Locate every blood parasite and identify its species.
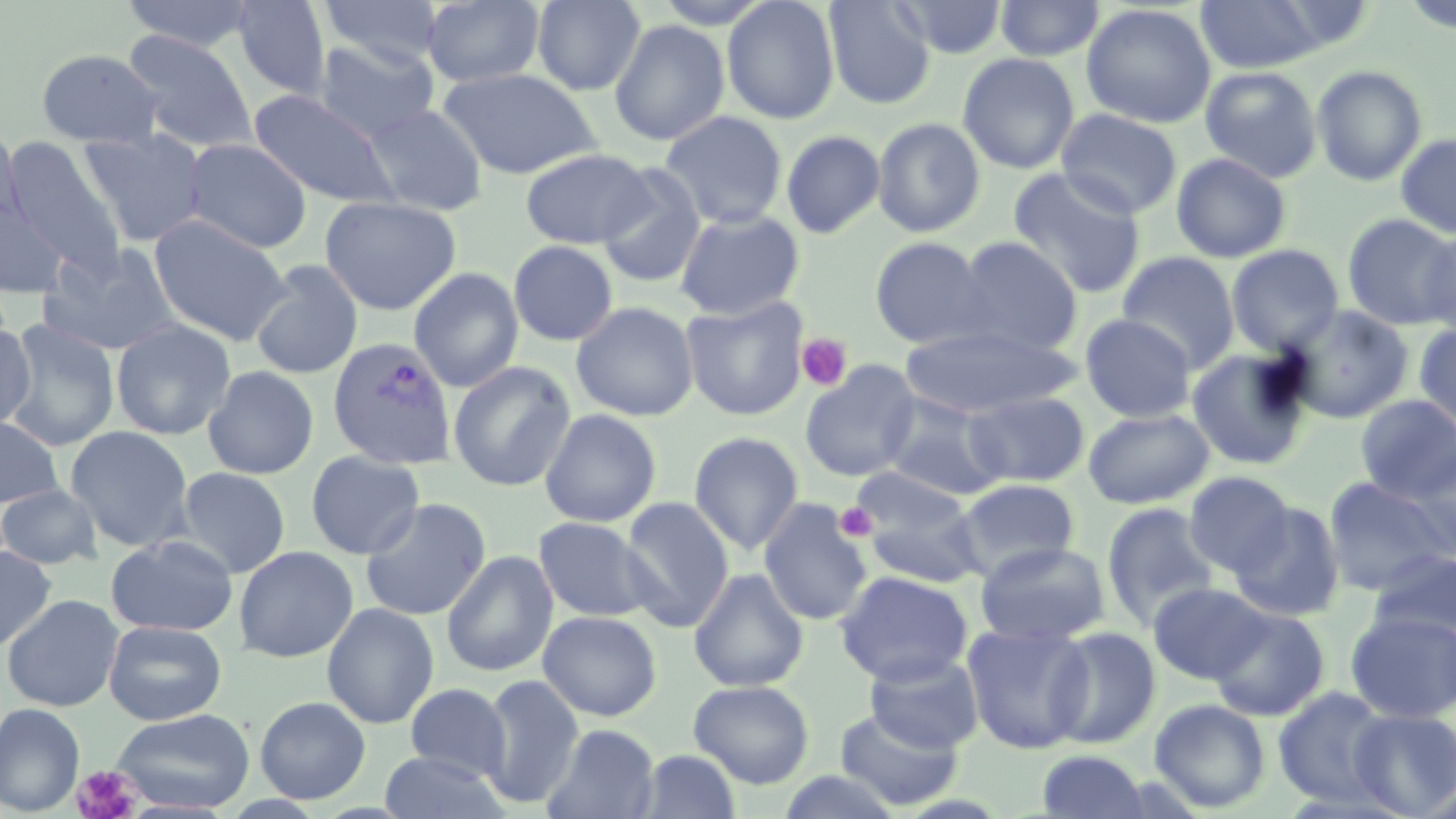
Approximate bounding boxes as named x1/y1/x2/y2 corners in pixels.
Plasmodium vivax-infected red blood cells: (x1=327, y1=334, x2=457, y2=469).
No Plasmodium falciparum, Plasmodium ovale, Plasmodium malariae, Babesia divergens, or Trypanosoma brucei observed.

Uninfected red blood cell locations: (x1=121, y1=0, x2=259, y2=52), (x1=231, y1=0, x2=332, y2=99), (x1=318, y1=0, x2=445, y2=68), (x1=531, y1=0, x2=646, y2=95), (x1=721, y1=0, x2=840, y2=124), (x1=823, y1=0, x2=935, y2=109), (x1=892, y1=0, x2=1008, y2=59), (x1=994, y1=0, x2=1105, y2=62), (x1=1195, y1=0, x2=1325, y2=73), (x1=421, y1=1, x2=545, y2=88), (x1=650, y1=1, x2=777, y2=28), (x1=1081, y1=3, x2=1217, y2=128), (x1=609, y1=19, x2=730, y2=146), (x1=121, y1=30, x2=258, y2=155), (x1=314, y1=37, x2=440, y2=142), (x1=36, y1=48, x2=163, y2=148), (x1=957, y1=52, x2=1080, y2=174), (x1=1311, y1=64, x2=1427, y2=187), (x1=1199, y1=66, x2=1323, y2=183), (x1=437, y1=67, x2=601, y2=179), (x1=248, y1=89, x2=397, y2=208), (x1=362, y1=103, x2=487, y2=216), (x1=1055, y1=108, x2=1182, y2=218), (x1=659, y1=111, x2=788, y2=229), (x1=872, y1=117, x2=987, y2=238), (x1=78, y1=126, x2=209, y2=247), (x1=0, y1=128, x2=24, y2=234), (x1=781, y1=129, x2=885, y2=239), (x1=1395, y1=132, x2=1456, y2=239), (x1=3, y1=137, x2=127, y2=277), (x1=182, y1=137, x2=313, y2=254), (x1=520, y1=147, x2=653, y2=249), (x1=1171, y1=152, x2=1291, y2=263), (x1=594, y1=165, x2=707, y2=290), (x1=1008, y1=167, x2=1147, y2=298), (x1=319, y1=195, x2=461, y2=316), (x1=1, y1=197, x2=69, y2=298), (x1=675, y1=208, x2=805, y2=320), (x1=149, y1=213, x2=291, y2=346), (x1=1341, y1=213, x2=1455, y2=330), (x1=1420, y1=227, x2=1456, y2=338), (x1=868, y1=236, x2=993, y2=349), (x1=955, y1=236, x2=1083, y2=355), (x1=508, y1=240, x2=618, y2=347), (x1=39, y1=243, x2=183, y2=356), (x1=1226, y1=244, x2=1344, y2=358), (x1=1117, y1=252, x2=1240, y2=370), (x1=249, y1=260, x2=364, y2=380), (x1=408, y1=267, x2=524, y2=393), (x1=681, y1=296, x2=809, y2=421), (x1=571, y1=301, x2=699, y2=421), (x1=1284, y1=304, x2=1414, y2=423), (x1=1080, y1=313, x2=1197, y2=421), (x1=2, y1=319, x2=120, y2=452), (x1=111, y1=319, x2=236, y2=440), (x1=0, y1=320, x2=36, y2=432), (x1=1413, y1=323, x2=1456, y2=427), (x1=899, y1=324, x2=1077, y2=419), (x1=1187, y1=347, x2=1313, y2=470), (x1=447, y1=360, x2=577, y2=492), (x1=799, y1=361, x2=923, y2=482), (x1=202, y1=365, x2=320, y2=480), (x1=964, y1=390, x2=1089, y2=487), (x1=1354, y1=394, x2=1456, y2=503), (x1=881, y1=396, x2=1006, y2=499), (x1=539, y1=408, x2=662, y2=527), (x1=1083, y1=408, x2=1214, y2=509), (x1=0, y1=415, x2=64, y2=510), (x1=64, y1=425, x2=194, y2=552), (x1=688, y1=431, x2=805, y2=555), (x1=1407, y1=449, x2=1455, y2=559), (x1=305, y1=450, x2=426, y2=560), (x1=175, y1=467, x2=291, y2=578), (x1=851, y1=467, x2=974, y2=548), (x1=1184, y1=471, x2=1295, y2=577), (x1=1323, y1=476, x2=1453, y2=595), (x1=953, y1=478, x2=1080, y2=579), (x1=0, y1=484, x2=103, y2=570), (x1=860, y1=488, x2=986, y2=588), (x1=620, y1=495, x2=735, y2=633), (x1=359, y1=496, x2=492, y2=621), (x1=758, y1=498, x2=873, y2=627), (x1=1102, y1=502, x2=1220, y2=631), (x1=1230, y1=502, x2=1346, y2=621), (x1=533, y1=516, x2=656, y2=622), (x1=105, y1=534, x2=238, y2=636), (x1=974, y1=541, x2=1110, y2=646), (x1=0, y1=545, x2=57, y2=652), (x1=233, y1=545, x2=359, y2=663), (x1=1365, y1=548, x2=1456, y2=646), (x1=440, y1=550, x2=558, y2=677), (x1=688, y1=568, x2=809, y2=692), (x1=834, y1=570, x2=973, y2=686), (x1=1149, y1=582, x2=1270, y2=685), (x1=1, y1=594, x2=124, y2=712), (x1=321, y1=602, x2=440, y2=729), (x1=1209, y1=607, x2=1330, y2=721), (x1=538, y1=610, x2=662, y2=721), (x1=1345, y1=612, x2=1456, y2=723), (x1=103, y1=619, x2=227, y2=725), (x1=963, y1=621, x2=1093, y2=754), (x1=1045, y1=625, x2=1161, y2=749), (x1=863, y1=652, x2=984, y2=754), (x1=479, y1=673, x2=584, y2=808), (x1=688, y1=679, x2=814, y2=788), (x1=404, y1=683, x2=512, y2=781), (x1=1272, y1=686, x2=1396, y2=808), (x1=254, y1=696, x2=372, y2=804), (x1=1149, y1=698, x2=1270, y2=812), (x1=0, y1=703, x2=85, y2=815), (x1=110, y1=707, x2=256, y2=813), (x1=833, y1=707, x2=964, y2=812), (x1=1349, y1=707, x2=1456, y2=817), (x1=543, y1=723, x2=661, y2=819), (x1=637, y1=749, x2=741, y2=818), (x1=1036, y1=750, x2=1151, y2=818), (x1=378, y1=751, x2=511, y2=819). Platelet locations: (x1=796, y1=333, x2=853, y2=392), (x1=835, y1=502, x2=878, y2=542), (x1=71, y1=765, x2=141, y2=819). Slide-level diagnosis: Plasmodium vivax. Image is 1456×819 pixels. 1000x magnification. Optical microscopy. Thin blood film. Single field of view. May-Grünwald-Giemsa stain.